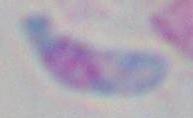 Toxoplasma gondii is shown. Micrograph. Captured at 1000x magnification.